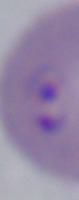
modality = micrograph
magnification = 1000x
identification = Babesia